Outline each blood parasite and name the species.
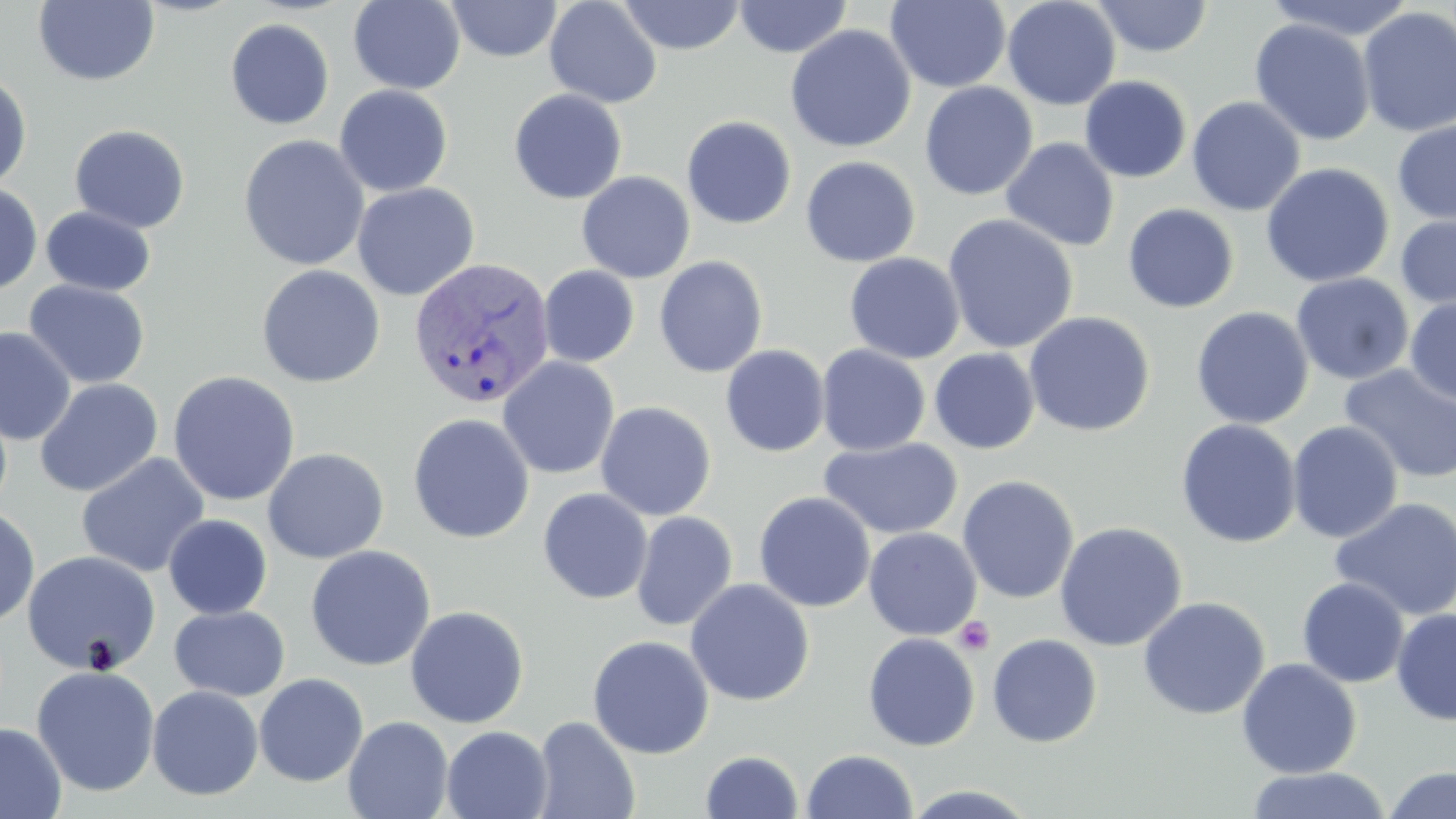

Approximate bounding boxes as (x1,y1)-(x2,y2) corner pairs in pixels.
Plasmodium vivax-infected red blood cells: (408,256)-(555,409).
No Plasmodium falciparum, Plasmodium ovale, Plasmodium malariae, Babesia divergens, or Trypanosoma brucei observed.

slide-level diagnosis = Plasmodium vivax
image size = 1456×819 pixels
field of view = one of a larger specimen
platelet locations = approximate bounding boxes as (x1,y1)-(x2,y2) corner pairs in pixels: (954,616)-(995,656)
uninfected red blood cell locations = approximate bounding boxes as (x1,y1)-(x2,y2) corner pairs in pixels: (348,0)-(466,95), (445,0)-(563,62), (544,0)-(663,108), (617,0)-(746,55), (733,0)-(853,58), (1002,0)-(1121,110), (1091,0)-(1215,58), (1261,0)-(1418,41), (33,1)-(160,87), (885,1)-(1011,92), (1357,7)-(1456,138), (225,18)-(334,130), (1249,18)-(1375,146), (785,24)-(917,153), (0,69)-(33,190), (1079,76)-(1192,183), (919,81)-(1038,201), (334,85)-(454,197), (508,89)-(628,204), (1186,96)-(1306,216), (681,115)-(797,229), (1392,118)-(1456,226), (69,124)-(191,234), (237,135)-(370,271), (1000,137)-(1120,252), (800,156)-(921,268), (1260,162)-(1395,288), (576,171)-(696,284), (0,181)-(42,295), (351,182)-(480,301), (1123,203)-(1239,314), (39,206)-(156,296), (1394,210)-(1456,314), (942,213)-(1079,354), (844,252)-(966,363), (654,256)-(768,378), (256,264)-(386,388), (538,265)-(640,367), (1290,273)-(1414,385), (24,279)-(150,389), (1404,297)-(1456,407), (1191,306)-(1314,429), (1023,311)-(1155,437), (0,327)-(77,445), (816,344)-(931,456), (720,345)-(830,457), (929,348)-(1040,454), (498,356)-(620,479), (1338,364)-(1456,484), (167,370)-(301,506), (34,378)-(163,497), (595,401)-(717,521), (407,413)-(535,544), (1176,419)-(1302,549), (1287,421)-(1403,543), (819,436)-(963,540), (262,447)-(389,563), (75,452)-(211,578), (957,475)-(1079,604), (537,488)-(653,604), (754,492)-(876,612), (1329,496)-(1456,621), (0,505)-(40,628), (631,511)-(738,631), (163,514)-(272,619), (1054,521)-(1187,651), (863,528)-(982,640), (305,545)-(436,672), (22,549)-(161,676), (1297,577)-(1409,688), (684,579)-(814,706), (1138,596)-(1270,719), (169,605)-(290,701), (405,605)-(530,728), (1391,608)-(1456,726), (862,632)-(981,751), (987,633)-(1102,747), (587,635)-(715,759), (1237,659)-(1362,779), (31,665)-(160,797), (254,673)-(369,787), (147,685)-(264,801), (532,715)-(640,819), (343,716)-(454,819), (0,722)-(66,819), (441,725)-(553,819), (801,749)-(918,818), (700,750)-(804,818), (1383,766)-(1455,818), (1245,767)-(1392,819)
magnification = 1000x
stain = May-Grünwald-Giemsa
modality = light microscopy
preparation = thin blood smear